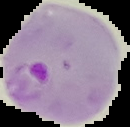

Summary:
  - Image size: 130×127 pixels
  - Preparation: thin blood smear
  - Result: Plasmodium parasites identified
  - Image type: segmented cell region on a black background